Assess this cell for malaria.
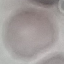

It is uninfected.

capture: smartphone camera at the microscope eyepiece
stain: Giemsa
preparation: thin blood smear
image_type: cell patch, automatically extracted from a larger field of view and resized to 64 × 64 pixels